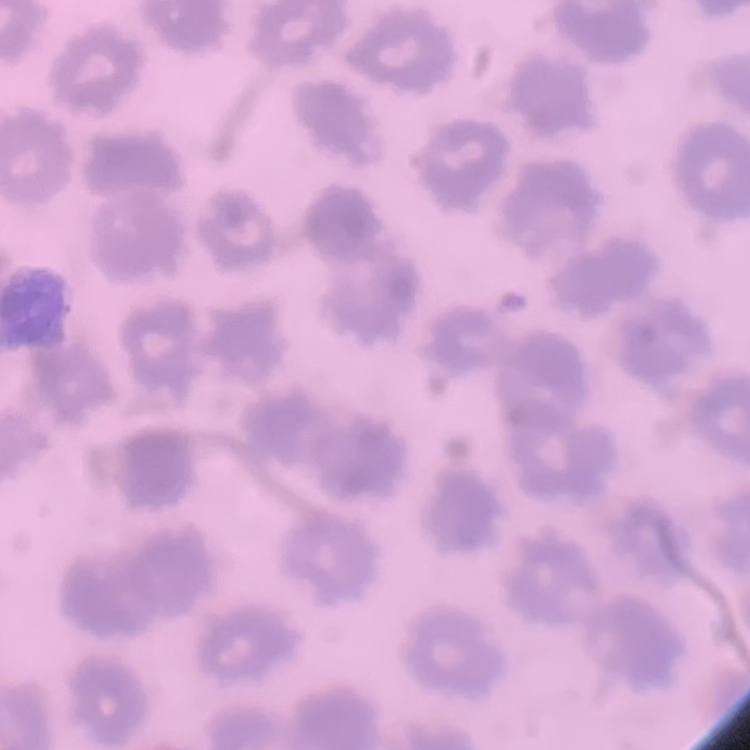

erythrocyte morphology = no rouleaux formation
stain = Field's or Giemsa
image type = one tile cut from a larger photomicrograph
preparation = thin peripheral smear